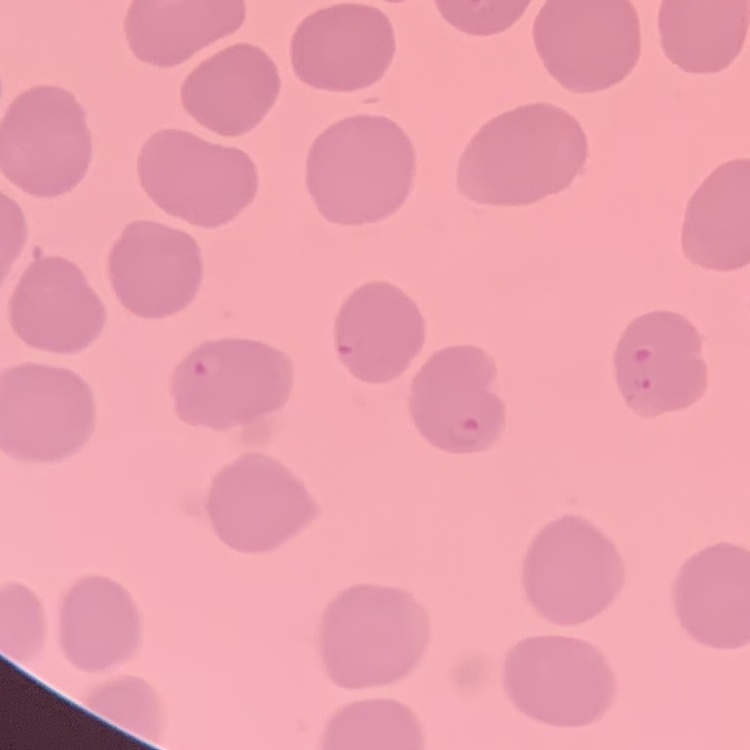

The red blood cells show no rouleaux formation. Stained with either Field's or Giemsa. Thin peripheral smear. One tile cut from a larger photomicrograph.